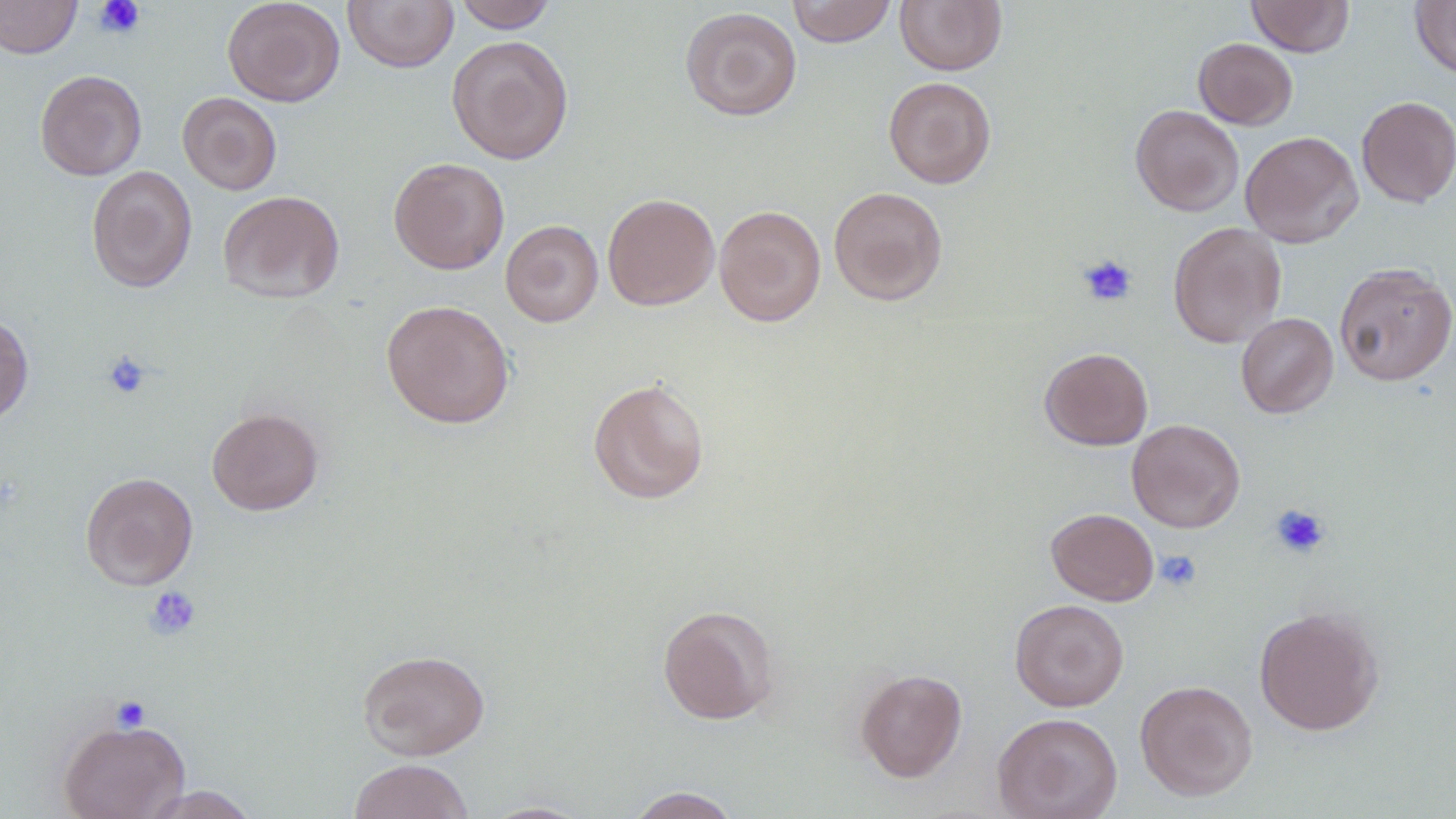

Summary:
  - Coordinate format: approximate bounding boxes as named x1/y1/x2/y2 corners in pixels
  - Platelet locations: (x1=94, y1=0, x2=145, y2=38), (x1=1078, y1=254, x2=1138, y2=307), (x1=102, y1=351, x2=152, y2=399), (x1=1270, y1=504, x2=1331, y2=558), (x1=1156, y1=550, x2=1202, y2=591), (x1=144, y1=586, x2=201, y2=639), (x1=110, y1=695, x2=151, y2=732)
  - Uninfected red blood cell locations: (x1=0, y1=0, x2=81, y2=59), (x1=222, y1=0, x2=345, y2=107), (x1=452, y1=0, x2=558, y2=32), (x1=787, y1=0, x2=896, y2=47), (x1=894, y1=0, x2=1007, y2=75), (x1=1246, y1=0, x2=1355, y2=57), (x1=343, y1=1, x2=458, y2=72), (x1=1410, y1=1, x2=1456, y2=79), (x1=679, y1=6, x2=802, y2=121), (x1=446, y1=35, x2=574, y2=164), (x1=1193, y1=37, x2=1297, y2=129), (x1=35, y1=69, x2=147, y2=180), (x1=883, y1=76, x2=997, y2=188), (x1=178, y1=92, x2=282, y2=195), (x1=1356, y1=95, x2=1456, y2=207), (x1=1130, y1=105, x2=1244, y2=217), (x1=1240, y1=130, x2=1363, y2=248), (x1=388, y1=157, x2=510, y2=275), (x1=86, y1=166, x2=198, y2=293), (x1=828, y1=186, x2=948, y2=306), (x1=217, y1=190, x2=345, y2=304), (x1=602, y1=193, x2=719, y2=311), (x1=714, y1=205, x2=826, y2=326), (x1=500, y1=220, x2=603, y2=327), (x1=1168, y1=222, x2=1287, y2=348), (x1=1334, y1=262, x2=1456, y2=386), (x1=380, y1=300, x2=515, y2=428), (x1=1236, y1=312, x2=1338, y2=418), (x1=0, y1=313, x2=34, y2=428), (x1=1039, y1=347, x2=1153, y2=451), (x1=587, y1=378, x2=710, y2=505), (x1=206, y1=407, x2=324, y2=515), (x1=1127, y1=418, x2=1246, y2=533), (x1=80, y1=471, x2=198, y2=590), (x1=1046, y1=508, x2=1159, y2=605), (x1=1010, y1=598, x2=1129, y2=712), (x1=657, y1=604, x2=779, y2=724), (x1=1254, y1=607, x2=1384, y2=735), (x1=357, y1=648, x2=490, y2=760), (x1=855, y1=668, x2=967, y2=782), (x1=1134, y1=680, x2=1258, y2=800), (x1=992, y1=712, x2=1123, y2=819), (x1=58, y1=717, x2=190, y2=819), (x1=348, y1=758, x2=474, y2=819), (x1=141, y1=785, x2=260, y2=818), (x1=626, y1=787, x2=741, y2=818), (x1=479, y1=800, x2=593, y2=818)
  - Slide-level diagnosis: no evidence of blood parasites
  - Stain: May-Grünwald-Giemsa
  - Modality: light microscopy
  - Image size: 1456×819 pixels
  - Magnification: 1000x
  - Field of view: one of a larger specimen
  - Preparation: thin blood smear